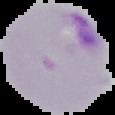
image size = 115×115 pixels
preparation = thin blood film
image type = segmented cell region on a black background
result = malaria parasites identified